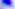

400x magnification. Photomicrograph. Toxoplasma gondii is shown.